Name the blood parasite species.
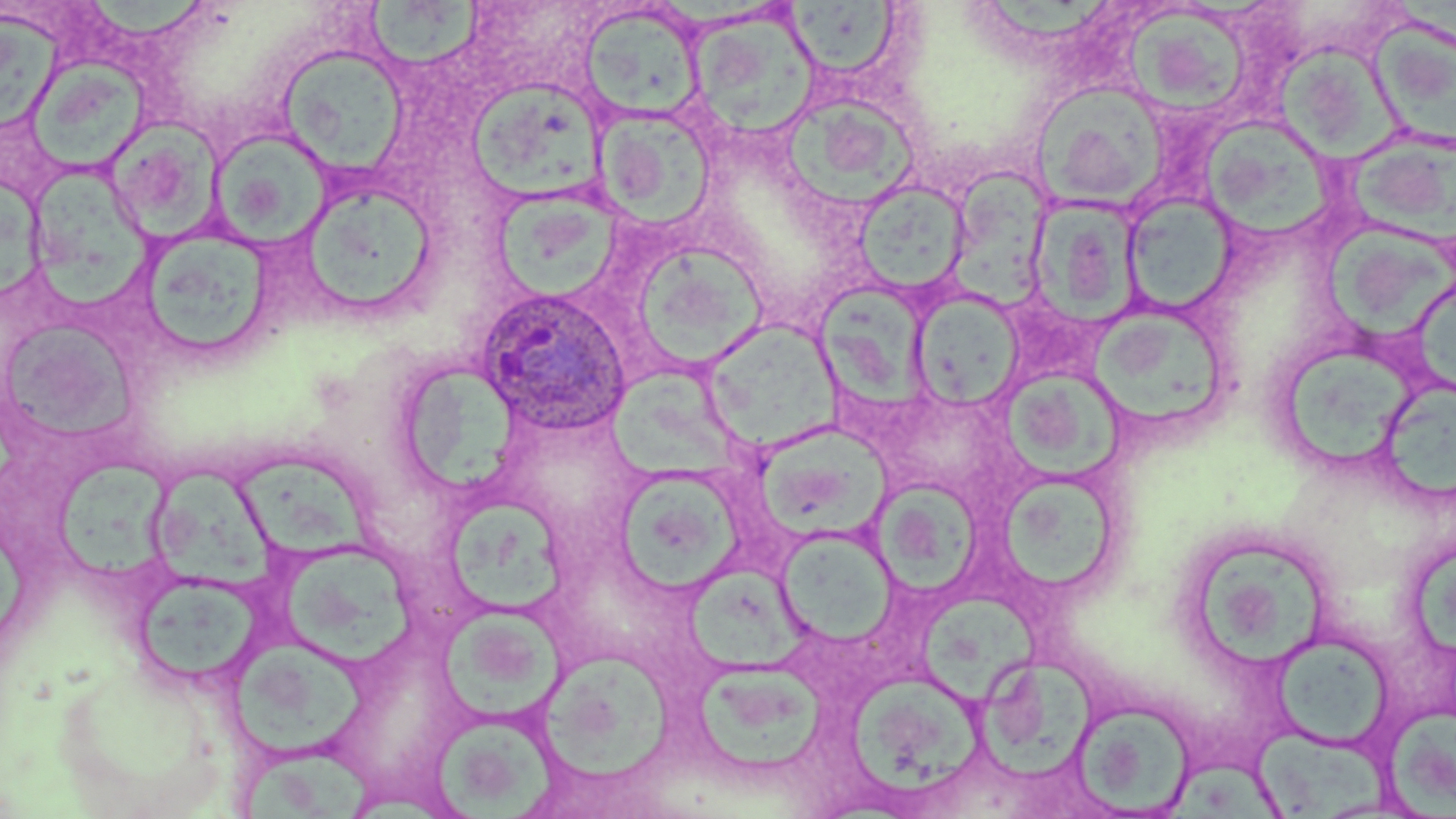
Plasmodium ovale.

Approximate bounding boxes as named x1/y1/x2/y2 corners in pixels. Plasmodium ovale-infected red blood cell locations: (x1=474, y1=286, x2=632, y2=438). Uninfected red blood cell locations: (x1=90, y1=0, x2=213, y2=44), (x1=365, y1=2, x2=484, y2=70), (x1=787, y1=4, x2=908, y2=79), (x1=580, y1=5, x2=705, y2=123), (x1=1127, y1=8, x2=1249, y2=114), (x1=688, y1=13, x2=821, y2=139), (x1=1, y1=15, x2=68, y2=132), (x1=1372, y1=18, x2=1456, y2=151), (x1=1278, y1=38, x2=1405, y2=164), (x1=278, y1=46, x2=410, y2=175), (x1=29, y1=52, x2=154, y2=179), (x1=471, y1=77, x2=606, y2=202), (x1=1035, y1=82, x2=1170, y2=208), (x1=786, y1=94, x2=924, y2=206), (x1=595, y1=107, x2=716, y2=227), (x1=1200, y1=115, x2=1336, y2=242), (x1=107, y1=120, x2=222, y2=240), (x1=213, y1=124, x2=335, y2=243), (x1=1351, y1=133, x2=1456, y2=240), (x1=29, y1=165, x2=157, y2=314), (x1=949, y1=167, x2=1048, y2=313), (x1=296, y1=179, x2=439, y2=323), (x1=853, y1=179, x2=972, y2=298), (x1=0, y1=180, x2=47, y2=301), (x1=496, y1=187, x2=627, y2=308), (x1=1122, y1=193, x2=1238, y2=314), (x1=1029, y1=199, x2=1140, y2=324), (x1=1317, y1=219, x2=1456, y2=341), (x1=147, y1=236, x2=272, y2=349), (x1=637, y1=239, x2=771, y2=373), (x1=815, y1=283, x2=933, y2=414), (x1=911, y1=291, x2=1026, y2=410), (x1=1097, y1=310, x2=1227, y2=432), (x1=701, y1=320, x2=839, y2=453), (x1=9, y1=324, x2=139, y2=446), (x1=1288, y1=345, x2=1418, y2=462), (x1=609, y1=364, x2=747, y2=482), (x1=409, y1=366, x2=520, y2=494), (x1=1000, y1=371, x2=1125, y2=483), (x1=1388, y1=372, x2=1456, y2=506), (x1=760, y1=422, x2=909, y2=546), (x1=59, y1=456, x2=169, y2=582), (x1=235, y1=459, x2=389, y2=564), (x1=150, y1=464, x2=284, y2=596), (x1=622, y1=475, x2=747, y2=593), (x1=997, y1=475, x2=1115, y2=592), (x1=873, y1=479, x2=980, y2=601), (x1=444, y1=499, x2=567, y2=617), (x1=776, y1=528, x2=898, y2=646), (x1=1409, y1=541, x2=1456, y2=658), (x1=1199, y1=542, x2=1326, y2=666), (x1=287, y1=550, x2=422, y2=671), (x1=688, y1=556, x2=807, y2=678), (x1=131, y1=570, x2=267, y2=691), (x1=922, y1=597, x2=1043, y2=710), (x1=444, y1=616, x2=571, y2=723), (x1=1272, y1=634, x2=1393, y2=748), (x1=546, y1=644, x2=674, y2=784), (x1=233, y1=645, x2=371, y2=759), (x1=971, y1=654, x2=1106, y2=793), (x1=693, y1=662, x2=830, y2=774), (x1=845, y1=672, x2=993, y2=805), (x1=1073, y1=701, x2=1196, y2=815), (x1=1389, y1=709, x2=1455, y2=813), (x1=433, y1=714, x2=556, y2=816), (x1=1253, y1=719, x2=1396, y2=819), (x1=241, y1=745, x2=383, y2=819), (x1=1172, y1=755, x2=1276, y2=819). Image is 1456×819 pixels. May-Grünwald-Giemsa stain. Thin blood film. One field of a larger specimen. Captured at 1000x magnification. Light microscopy.